Outline each uninfected red blood cell.
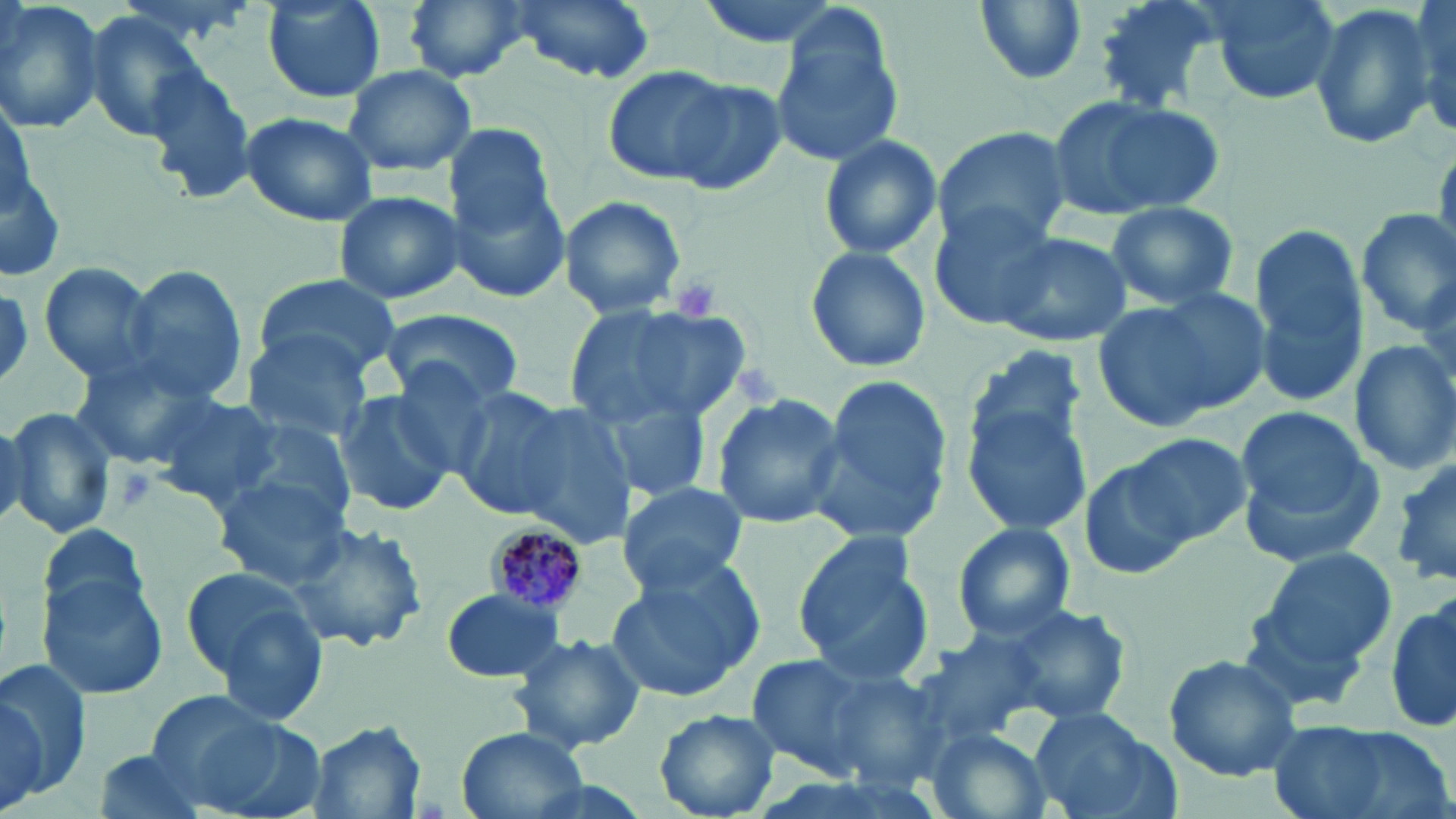

Approximate bounding boxes as [x1, y1, x2, y2] in pixels.
Uninfected red blood cells: [0, 0, 107, 137], [259, 0, 388, 104], [403, 0, 532, 85], [507, 0, 661, 87], [970, 0, 1089, 86], [1089, 0, 1227, 115], [1201, 0, 1342, 105], [1411, 0, 1455, 139], [1308, 2, 1439, 149], [80, 9, 206, 142], [767, 13, 907, 166], [138, 62, 256, 202], [339, 63, 477, 175], [602, 66, 740, 185], [660, 72, 789, 194], [1050, 93, 1224, 217], [240, 110, 379, 228], [442, 121, 559, 239], [932, 127, 1070, 249], [816, 133, 943, 261], [0, 141, 67, 287], [448, 163, 574, 304], [334, 189, 464, 307], [559, 196, 687, 318], [1104, 200, 1240, 312], [931, 202, 1061, 330], [1355, 207, 1456, 334], [1248, 223, 1368, 406], [984, 228, 1134, 351], [804, 244, 932, 374], [36, 261, 160, 386], [120, 266, 247, 406], [253, 273, 403, 378], [0, 284, 32, 391], [1094, 291, 1262, 431], [566, 301, 749, 429], [380, 307, 524, 409], [240, 330, 374, 446], [1349, 338, 1456, 475], [965, 345, 1089, 466], [67, 356, 210, 472], [807, 372, 951, 546], [448, 385, 573, 520], [332, 390, 456, 521], [150, 391, 284, 509], [711, 391, 846, 532], [591, 397, 715, 500], [506, 401, 639, 547], [964, 402, 1095, 533], [1, 406, 117, 540], [1240, 409, 1374, 517], [230, 417, 361, 531], [1128, 435, 1249, 546], [1081, 456, 1198, 582], [212, 471, 354, 590], [617, 481, 750, 593], [284, 518, 431, 657], [40, 520, 152, 622], [951, 522, 1074, 641], [793, 531, 937, 685], [1249, 544, 1397, 683], [182, 565, 326, 705], [607, 568, 757, 703], [38, 571, 171, 699], [440, 588, 566, 682], [1386, 596, 1456, 736], [991, 601, 1132, 726], [509, 631, 646, 752], [907, 634, 1046, 750], [1163, 652, 1302, 781], [744, 654, 886, 783], [1, 656, 92, 801], [820, 665, 952, 787], [1, 685, 52, 810], [149, 695, 323, 817], [1027, 705, 1170, 819], [655, 709, 780, 817], [1269, 721, 1446, 819], [306, 722, 428, 818], [454, 728, 589, 819], [927, 729, 1052, 819], [92, 751, 214, 819].

Summary:
  - Plasmodium malariae-infected red blood cell locations: [485, 520, 589, 617]
  - Platelet locations: [670, 273, 724, 323], [735, 366, 783, 407], [120, 470, 153, 511]
  - Slide-level diagnosis: Plasmodium malariae
  - Magnification: 1000x
  - Preparation: thin blood film
  - Modality: light microscopy
  - Stain: May-Grünwald-Giemsa
  - Image size: 1456×819 pixels
  - Field of view: single